Report the malaria status of this cell.
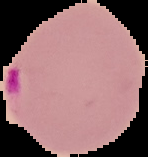

It is parasitized.

{
  "image_size": "148×157 pixels",
  "image_type": "segmented cell region with the area outside set to black",
  "preparation": "thin blood smear"
}